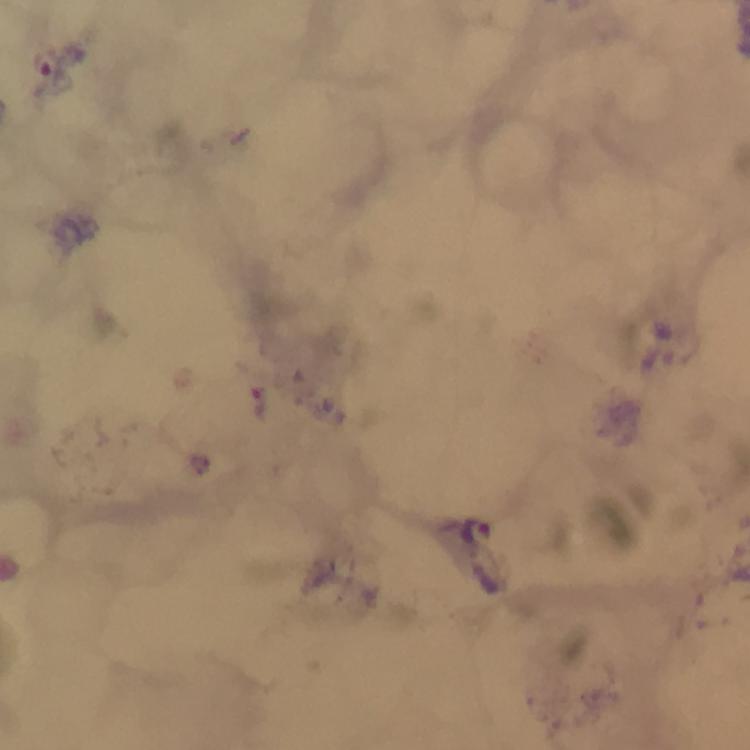

Approximate centers as {x, y} in pixels. Plasmodium parasite locations: {45, 66}, {258, 404}, {477, 530}. Immersion oil was used. Giemsa-stained preparation. 100x magnification. Thick smear. From a diagnostic examination for malaria. A crop from one field of view. Image is 750×750 pixels. Photographed through the microscope with a smartphone camera.